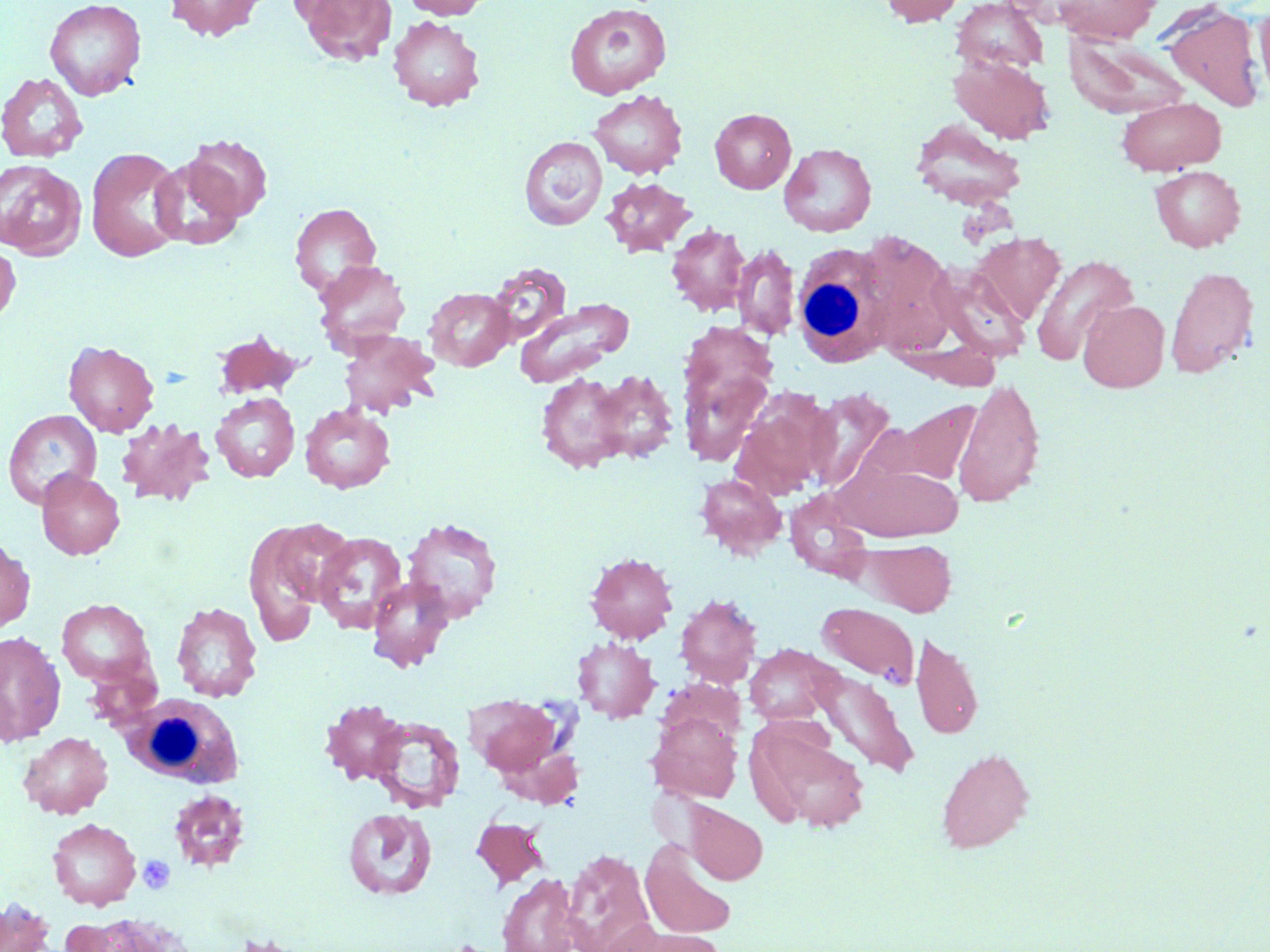

Approximate bounding boxes as named x1/y1/x2/y2 corners in pixels. White blood cell locations: (x1=791, y1=243, x2=891, y2=367), (x1=123, y1=694, x2=244, y2=789). Uninfected red blood cell locations: (x1=44, y1=0, x2=146, y2=100), (x1=165, y1=0, x2=267, y2=40), (x1=298, y1=0, x2=397, y2=66), (x1=404, y1=0, x2=492, y2=19), (x1=879, y1=0, x2=966, y2=27), (x1=1052, y1=0, x2=1161, y2=44), (x1=952, y1=1, x2=1049, y2=75), (x1=1162, y1=1, x2=1264, y2=112), (x1=1254, y1=2, x2=1270, y2=105), (x1=564, y1=3, x2=672, y2=100), (x1=387, y1=16, x2=485, y2=111), (x1=1064, y1=34, x2=1189, y2=119), (x1=950, y1=54, x2=1055, y2=144), (x1=0, y1=71, x2=88, y2=163), (x1=589, y1=89, x2=688, y2=179), (x1=1116, y1=97, x2=1226, y2=174), (x1=710, y1=108, x2=796, y2=193), (x1=910, y1=119, x2=1027, y2=210), (x1=184, y1=135, x2=273, y2=220), (x1=519, y1=136, x2=607, y2=230), (x1=779, y1=142, x2=877, y2=237), (x1=86, y1=147, x2=186, y2=263), (x1=150, y1=157, x2=244, y2=250), (x1=0, y1=159, x2=86, y2=259), (x1=1149, y1=165, x2=1246, y2=251), (x1=601, y1=176, x2=696, y2=256), (x1=290, y1=203, x2=381, y2=295), (x1=665, y1=223, x2=751, y2=316), (x1=971, y1=232, x2=1065, y2=324), (x1=862, y1=233, x2=959, y2=353), (x1=0, y1=242, x2=20, y2=325), (x1=732, y1=243, x2=800, y2=341), (x1=1031, y1=254, x2=1138, y2=365), (x1=313, y1=259, x2=411, y2=354), (x1=486, y1=261, x2=572, y2=345), (x1=927, y1=264, x2=1032, y2=363), (x1=1164, y1=265, x2=1259, y2=378), (x1=424, y1=287, x2=515, y2=371), (x1=512, y1=298, x2=633, y2=387), (x1=1078, y1=299, x2=1170, y2=392), (x1=338, y1=329, x2=440, y2=418), (x1=211, y1=330, x2=303, y2=400), (x1=63, y1=340, x2=159, y2=437), (x1=680, y1=352, x2=775, y2=469), (x1=581, y1=368, x2=682, y2=466), (x1=532, y1=369, x2=646, y2=474), (x1=953, y1=377, x2=1045, y2=509), (x1=805, y1=388, x2=897, y2=493), (x1=730, y1=389, x2=833, y2=500), (x1=211, y1=392, x2=300, y2=482), (x1=897, y1=399, x2=982, y2=485), (x1=299, y1=403, x2=395, y2=494), (x1=3, y1=409, x2=102, y2=508), (x1=116, y1=417, x2=214, y2=507), (x1=839, y1=461, x2=964, y2=541), (x1=36, y1=469, x2=125, y2=559), (x1=695, y1=473, x2=787, y2=559), (x1=784, y1=488, x2=875, y2=582), (x1=253, y1=517, x2=348, y2=630), (x1=402, y1=517, x2=503, y2=623), (x1=313, y1=531, x2=408, y2=634), (x1=863, y1=539, x2=957, y2=616), (x1=0, y1=540, x2=35, y2=632), (x1=584, y1=551, x2=678, y2=643), (x1=367, y1=577, x2=454, y2=671), (x1=675, y1=594, x2=762, y2=688), (x1=56, y1=598, x2=155, y2=686), (x1=170, y1=601, x2=263, y2=702), (x1=816, y1=602, x2=920, y2=686), (x1=0, y1=631, x2=65, y2=744), (x1=911, y1=631, x2=983, y2=740), (x1=572, y1=636, x2=660, y2=723), (x1=744, y1=644, x2=838, y2=725), (x1=810, y1=669, x2=920, y2=778), (x1=466, y1=695, x2=564, y2=778), (x1=320, y1=699, x2=409, y2=784), (x1=647, y1=710, x2=743, y2=803), (x1=368, y1=715, x2=465, y2=813), (x1=748, y1=722, x2=870, y2=833), (x1=19, y1=732, x2=112, y2=818), (x1=936, y1=747, x2=1035, y2=854), (x1=168, y1=789, x2=251, y2=872), (x1=686, y1=803, x2=767, y2=884), (x1=343, y1=808, x2=437, y2=900), (x1=471, y1=816, x2=549, y2=889), (x1=46, y1=818, x2=141, y2=910), (x1=640, y1=837, x2=737, y2=940), (x1=562, y1=848, x2=655, y2=952), (x1=497, y1=873, x2=583, y2=951), (x1=1, y1=899, x2=56, y2=952), (x1=74, y1=913, x2=191, y2=952), (x1=609, y1=924, x2=720, y2=952), (x1=222, y1=931, x2=323, y2=952), (x1=431, y1=939, x2=516, y2=952). Platelet locations: (x1=137, y1=854, x2=175, y2=894). Slide-level diagnosis: no evidence of blood parasites. Captured at 1000x magnification. Single field of view. Optical microscopy. Thin blood smear. May-Grünwald-Giemsa-stained preparation. Image is 1270×952 pixels.